Classify this cell by malaria status.
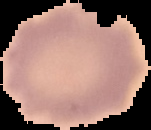
It is uninfected.

From a thin blood film. Image is 151×130 pixels. Segmented cell region on a black background.